Locate every Plasmodium falciparum-infected red blood cell.
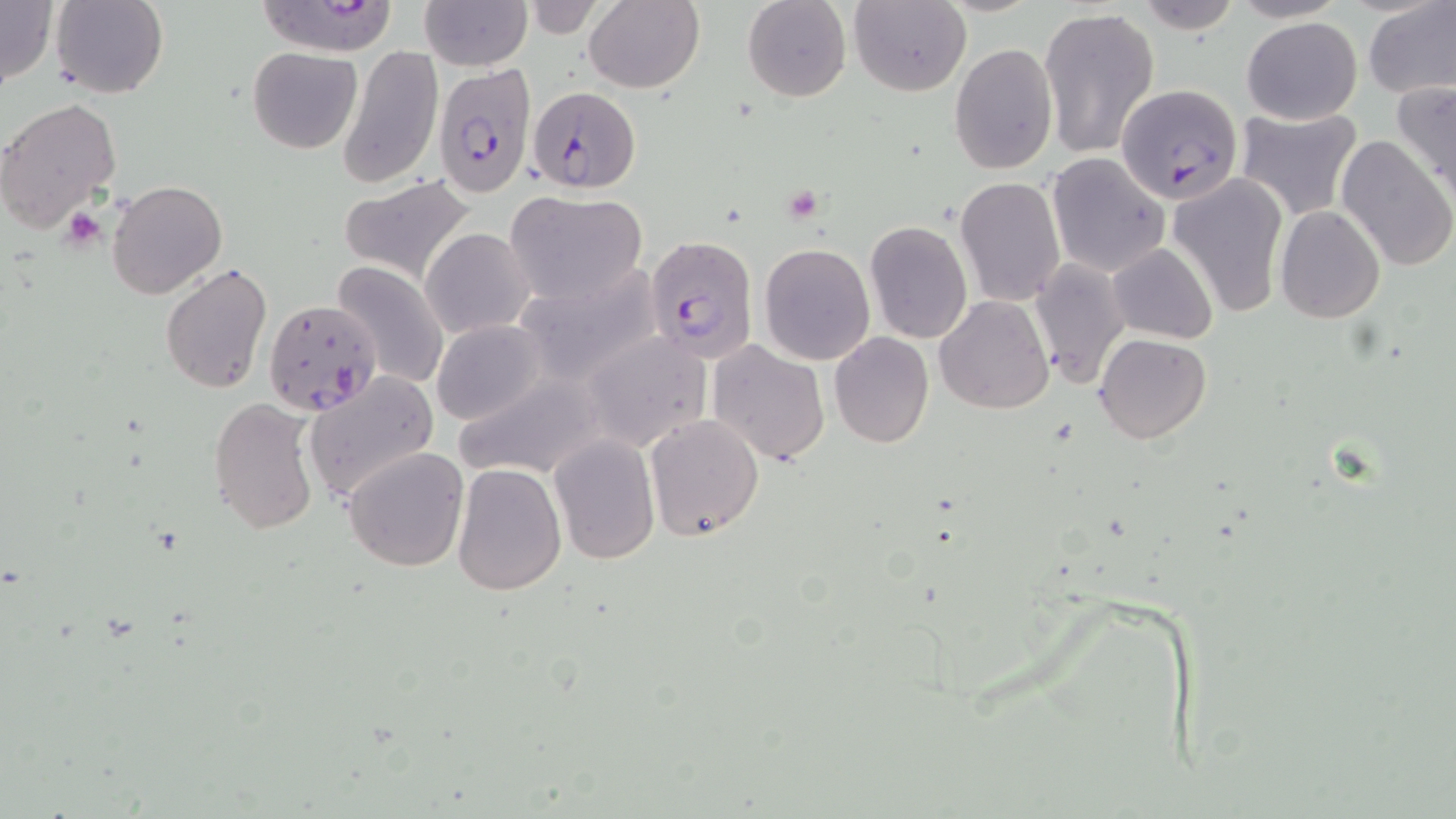

Approximate bounding boxes as (x1,y1)-(x2,y2) corner pairs in pixels.
Plasmodium falciparum-infected red blood cells: (253,3)-(403,57), (434,63)-(537,195), (526,85)-(640,194), (1117,85)-(1245,204), (646,234)-(759,363), (262,298)-(383,418).

{
  "slide_level_diagnosis": "Plasmodium falciparum",
  "stain": "May-Grünwald-Giemsa",
  "magnification": "1000x",
  "platelet_locations": "approximate bounding boxes as (x1,y1)-(x2,y2) corner pairs in pixels: (60,209)-(106,251)",
  "field_of_view": "single",
  "uninfected_red_blood_cell_locations": "approximate bounding boxes as (x1,y1)-(x2,y2) corner pairs in pixels: (0,0)-(58,91), (50,0)-(168,100), (419,0)-(532,71), (584,0)-(706,94), (742,0)-(852,102), (849,0)-(970,95), (1132,0)-(1241,35), (1364,1)-(1456,98), (514,3)-(610,38), (1039,5)-(1158,160), (1242,17)-(1362,124), (949,42)-(1059,176), (337,45)-(444,189), (247,46)-(361,154), (1391,78)-(1456,203), (0,95)-(122,232), (1237,107)-(1360,219), (1335,134)-(1455,272), (1048,153)-(1169,277), (1167,172)-(1287,317), (336,174)-(480,286), (954,175)-(1066,306), (106,178)-(229,300), (504,192)-(649,306), (1275,205)-(1385,323), (863,219)-(972,345), (421,227)-(535,337), (1107,241)-(1216,344), (759,243)-(875,364), (1028,257)-(1131,389), (332,260)-(449,388), (159,261)-(273,396), (512,265)-(663,388), (934,296)-(1053,413), (431,320)-(547,426), (579,332)-(711,453), (829,332)-(933,448), (1094,333)-(1211,443), (707,340)-(830,465), (451,371)-(605,482), (304,372)-(439,503), (208,396)-(323,538), (643,413)-(764,541), (548,435)-(660,566), (342,446)-(469,571), (451,461)-(564,596)",
  "image_size": "1456×819 pixels",
  "preparation": "thin blood smear",
  "modality": "optical microscopy"
}